Report the malaria status of this cell.
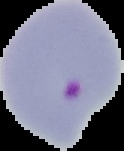
It is parasitized.

Summary:
  - Image size: 124×151 pixels
  - Image type: segmented cell region with the area outside set to black
  - Preparation: thin blood film